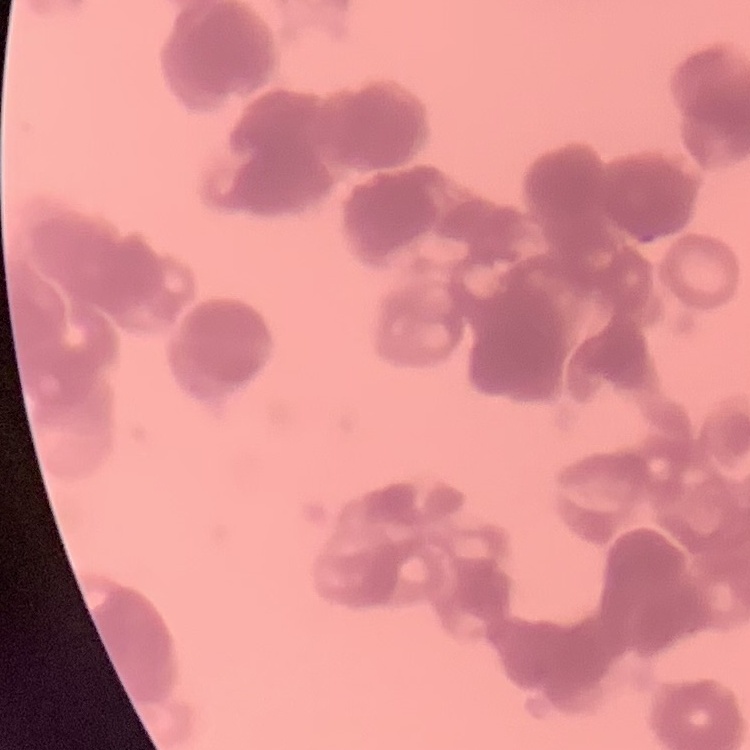

Summary:
  - Erythrocyte morphology: rouleaux formation
  - Stain: Field's or Giemsa
  - Image type: one tile cut from a larger photomicrograph
  - Preparation: thin blood film